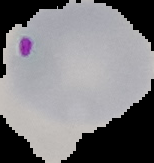

preparation: thin blood smear
image_type: segmented cell region on a black background
image_size: 154×163 pixels
result: Plasmodium parasites identified